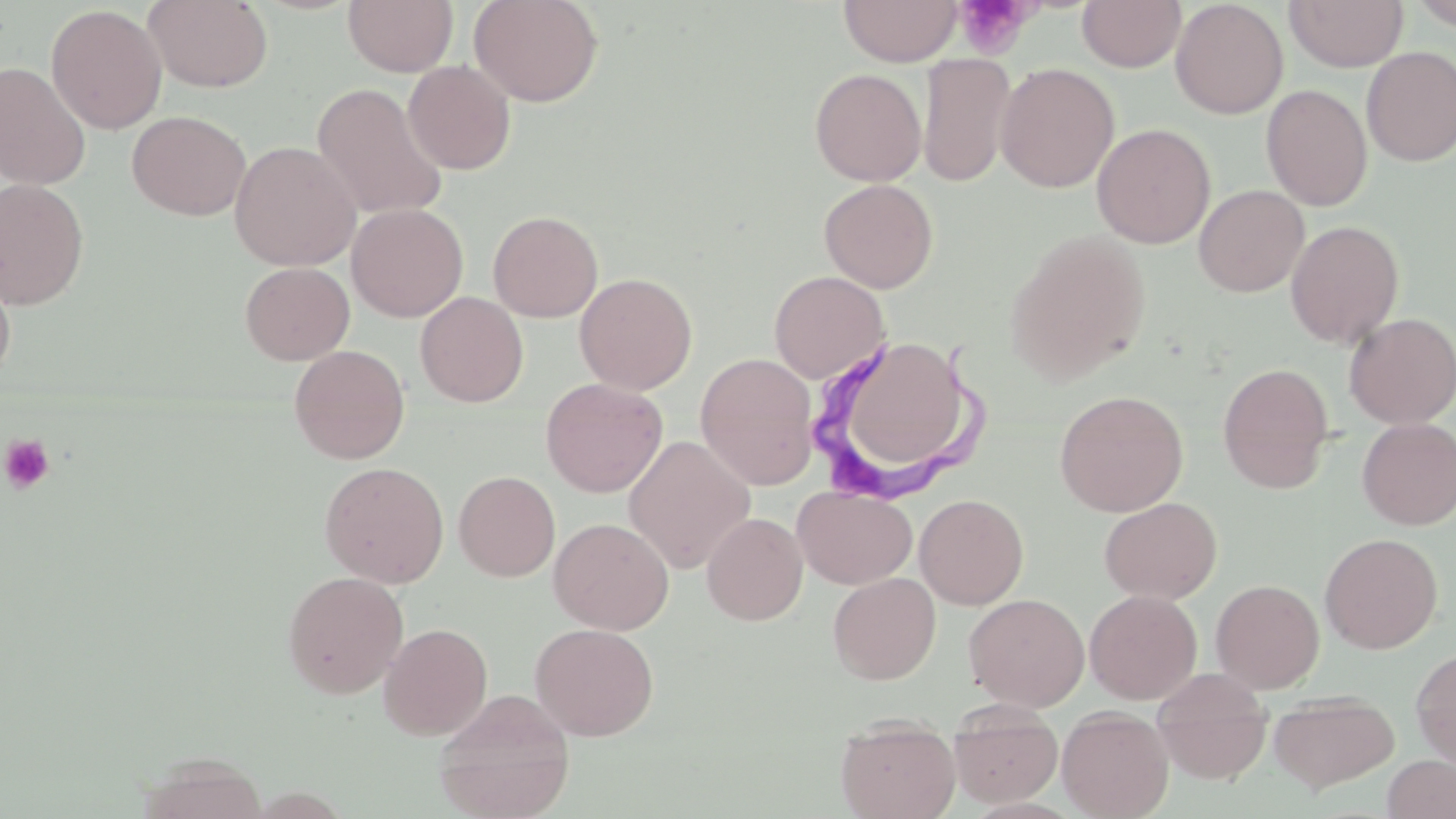

slide-level diagnosis = Trypanosoma brucei
stain = May-Grünwald-Giemsa
magnification = 1000x
uninfected red blood cell locations = approximate bounding boxes as (x1, y1, x2, y2) in pixels: (143, 0, 273, 92), (343, 0, 458, 76), (468, 0, 604, 108), (838, 0, 964, 66), (1077, 0, 1186, 72), (1081, 0, 1261, 103), (1170, 0, 1288, 119), (1285, 0, 1407, 72), (1409, 0, 1456, 31), (46, 4, 167, 134), (1360, 46, 1456, 166), (918, 52, 1016, 188), (403, 60, 516, 175), (0, 61, 92, 190), (995, 62, 1120, 193), (809, 68, 927, 186), (312, 83, 448, 220), (1261, 84, 1373, 212), (126, 110, 252, 220), (1092, 123, 1215, 249), (229, 141, 361, 270), (0, 178, 90, 310), (819, 178, 938, 293), (1193, 184, 1309, 297), (346, 203, 468, 322), (487, 210, 603, 322), (1285, 220, 1405, 349), (1008, 230, 1151, 383), (240, 261, 355, 365), (0, 264, 16, 386), (769, 270, 890, 383), (574, 271, 697, 395), (415, 291, 528, 407), (1343, 312, 1456, 429), (851, 338, 959, 464), (289, 344, 410, 464), (695, 353, 819, 489), (1218, 362, 1334, 493), (540, 378, 668, 498), (1054, 389, 1189, 517), (1357, 418, 1456, 530), (623, 435, 756, 573), (319, 461, 449, 588), (453, 470, 560, 582), (793, 486, 917, 589), (914, 493, 1029, 609), (1099, 496, 1222, 604), (702, 512, 808, 625), (549, 517, 674, 634), (1320, 533, 1442, 653), (282, 570, 409, 700), (828, 572, 941, 684), (1211, 579, 1324, 693), (1084, 589, 1202, 704), (964, 593, 1090, 711), (378, 622, 493, 740), (530, 623, 659, 741), (1411, 647, 1456, 767), (1152, 669, 1273, 785), (434, 689, 575, 819), (1269, 690, 1400, 793), (948, 705, 1063, 808), (1057, 707, 1174, 819), (835, 717, 960, 819), (1382, 755, 1456, 819)
modality = optical microscopy
image size = 1456×819 pixels
Trypanosoma brucei locations = approximate bounding boxes as (x1, y1, x2, y2) in pixels: (807, 326, 997, 506)
platelet locations = approximate bounding boxes as (x1, y1, x2, y2) in pixels: (955, 0, 1035, 59), (0, 433, 56, 494)
preparation = thin blood film
field of view = one of a larger specimen